Assess this cell for malaria.
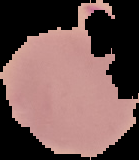
Uninfected.

Summary:
  - Image type: segmented cell region with the area outside set to black
  - Image size: 139×160 pixels
  - Preparation: thin blood smear